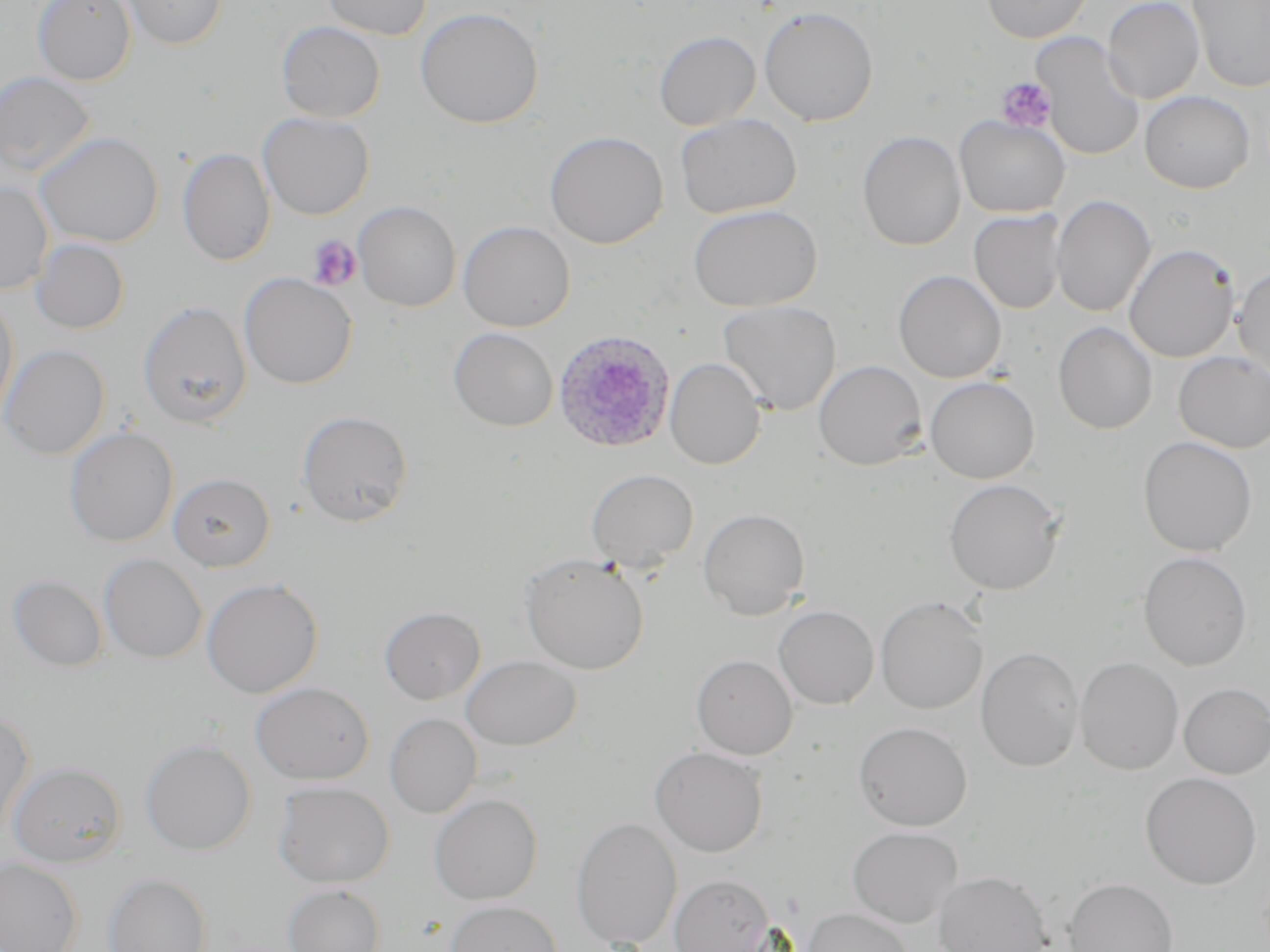

{
  "plasmodium_ovale_infected_red_blood_cell_locations": "approximate bounding boxes as named x1/y1/x2/y2 corners in pixels: (x1=553, y1=331, x2=675, y2=454)",
  "slide_level_diagnosis": "Plasmodium ovale",
  "stain": "May-Grünwald-Giemsa",
  "preparation": "thin blood film",
  "modality": "optical microscopy",
  "platelet_locations": "approximate bounding boxes as named x1/y1/x2/y2 corners in pixels: (x1=995, y1=77, x2=1057, y2=133), (x1=307, y1=235, x2=362, y2=291)",
  "uninfected_red_blood_cell_locations": "approximate bounding boxes as named x1/y1/x2/y2 corners in pixels: (x1=32, y1=0, x2=136, y2=86), (x1=120, y1=0, x2=229, y2=50), (x1=320, y1=0, x2=432, y2=40), (x1=981, y1=0, x2=1092, y2=43), (x1=1102, y1=0, x2=1205, y2=104), (x1=1187, y1=0, x2=1270, y2=94), (x1=759, y1=6, x2=879, y2=126), (x1=415, y1=7, x2=544, y2=129), (x1=276, y1=21, x2=386, y2=123), (x1=654, y1=31, x2=761, y2=131), (x1=1031, y1=32, x2=1145, y2=161), (x1=0, y1=71, x2=95, y2=178), (x1=1140, y1=90, x2=1255, y2=193), (x1=257, y1=112, x2=374, y2=220), (x1=674, y1=113, x2=802, y2=218), (x1=954, y1=115, x2=1070, y2=218), (x1=544, y1=130, x2=668, y2=249), (x1=858, y1=131, x2=966, y2=251), (x1=34, y1=132, x2=164, y2=248), (x1=177, y1=147, x2=275, y2=266), (x1=0, y1=180, x2=53, y2=294), (x1=1051, y1=194, x2=1156, y2=317), (x1=354, y1=201, x2=461, y2=311), (x1=688, y1=204, x2=822, y2=311), (x1=969, y1=209, x2=1067, y2=314), (x1=458, y1=220, x2=575, y2=332), (x1=31, y1=238, x2=129, y2=334), (x1=1124, y1=243, x2=1240, y2=363), (x1=1234, y1=265, x2=1270, y2=379), (x1=893, y1=270, x2=1006, y2=383), (x1=239, y1=273, x2=357, y2=389), (x1=0, y1=295, x2=19, y2=426), (x1=137, y1=300, x2=252, y2=429), (x1=718, y1=300, x2=842, y2=416), (x1=1053, y1=321, x2=1157, y2=434), (x1=449, y1=327, x2=558, y2=431), (x1=1, y1=344, x2=110, y2=459), (x1=1173, y1=352, x2=1270, y2=452), (x1=665, y1=358, x2=766, y2=469), (x1=813, y1=360, x2=927, y2=470), (x1=925, y1=376, x2=1040, y2=483), (x1=296, y1=409, x2=414, y2=527), (x1=64, y1=427, x2=179, y2=547), (x1=1138, y1=436, x2=1257, y2=556), (x1=586, y1=468, x2=698, y2=572), (x1=168, y1=472, x2=275, y2=571), (x1=943, y1=478, x2=1064, y2=595), (x1=699, y1=508, x2=810, y2=620), (x1=1138, y1=551, x2=1252, y2=671), (x1=521, y1=553, x2=649, y2=675), (x1=99, y1=554, x2=207, y2=663), (x1=8, y1=574, x2=108, y2=672), (x1=201, y1=578, x2=323, y2=698), (x1=875, y1=596, x2=988, y2=714), (x1=773, y1=605, x2=879, y2=709), (x1=379, y1=606, x2=486, y2=704), (x1=975, y1=646, x2=1084, y2=772), (x1=461, y1=654, x2=581, y2=751), (x1=691, y1=654, x2=797, y2=760), (x1=1075, y1=656, x2=1184, y2=775), (x1=250, y1=682, x2=374, y2=784), (x1=1179, y1=683, x2=1270, y2=779), (x1=0, y1=710, x2=35, y2=838), (x1=384, y1=713, x2=481, y2=818), (x1=854, y1=721, x2=972, y2=831), (x1=140, y1=739, x2=256, y2=855), (x1=649, y1=746, x2=768, y2=857), (x1=7, y1=761, x2=126, y2=867), (x1=1141, y1=772, x2=1262, y2=889), (x1=273, y1=781, x2=395, y2=887), (x1=429, y1=793, x2=543, y2=905), (x1=571, y1=817, x2=682, y2=949), (x1=847, y1=826, x2=963, y2=928), (x1=0, y1=858, x2=83, y2=952), (x1=933, y1=871, x2=1052, y2=952), (x1=103, y1=872, x2=212, y2=952), (x1=670, y1=874, x2=774, y2=952), (x1=1064, y1=877, x2=1178, y2=952), (x1=282, y1=884, x2=386, y2=952), (x1=445, y1=900, x2=563, y2=952), (x1=802, y1=907, x2=915, y2=952)",
  "field_of_view": "one of a larger specimen",
  "image_size": "1270×952 pixels",
  "magnification": "1000x"
}